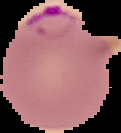

From a thin blood film. Cell region segmented out of the field of view; the surrounding area is masked to black. Image is 121×133 pixels. Malaria status: parasitized.